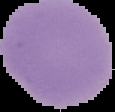

The area outside the segmented cell region is set to black. Result: negative for malaria parasites. From a thin blood film. Image is 115×112 pixels.